Report the malaria status of this cell.
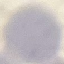

It is uninfected.

Acquired by smartphone through the microscope eyepiece. Automatically extracted cell patch, resized to 64 × 64 pixels. Thin blood film. Giemsa stain.